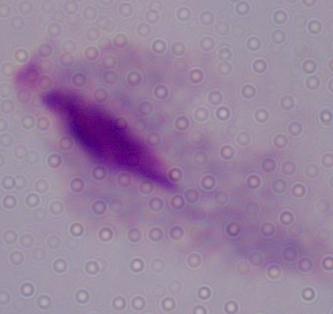

Micrograph. 1000x magnification. A trichomonad is seen.